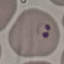
Result: malaria parasites detected. Automatically extracted cell patch, resized to 64 × 64 pixels. Giemsa stain. Thin blood film. Acquired by smartphone through the microscope eyepiece.